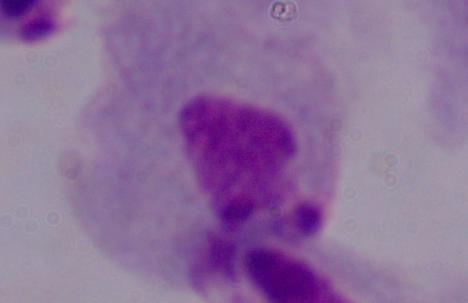
Summary:
  - Identification: trichomonad
  - Magnification: 1000x
  - Modality: micrograph